Assess this cell for malaria.
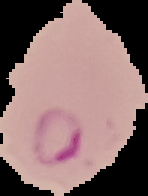

Parasitized.

image size = 148×196 pixels
image type = segmented cell region on a black background
preparation = thin blood smear